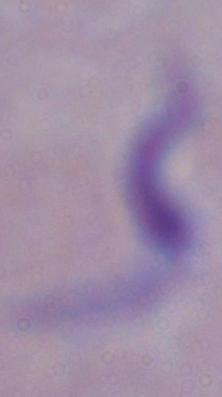

modality = photomicrograph
identification = trypanosome
magnification = 1000x